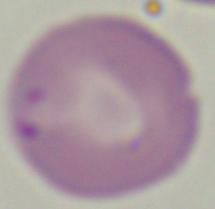 A Babesia parasite is seen. Micrograph. Captured at 1000x magnification.